State the blood parasite species.
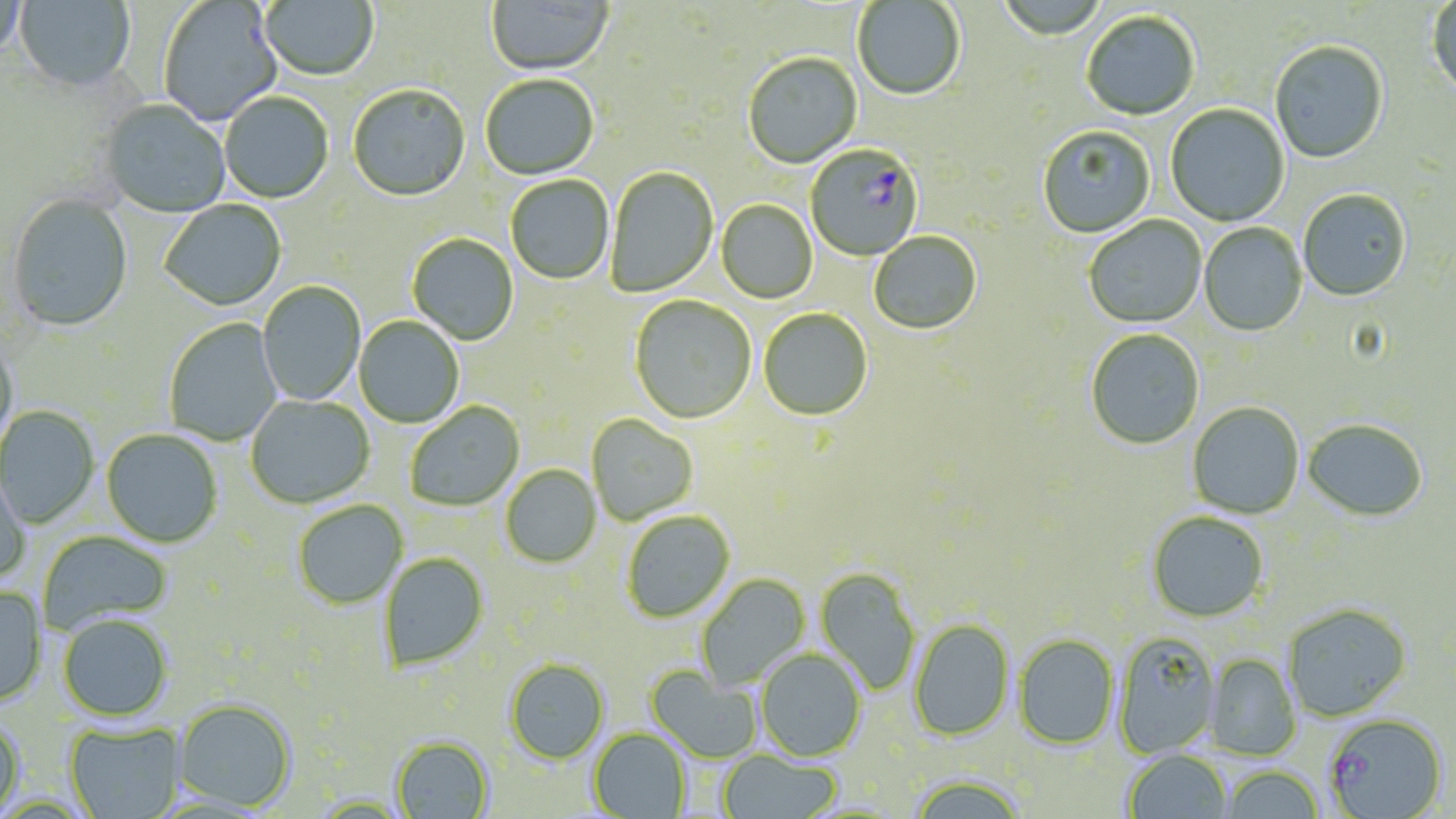
Plasmodium falciparum.

Approximate bounding boxes as [x1, y1, x2, y2] in pixels. Uninfected red blood cell locations: [15, 0, 136, 94], [260, 0, 378, 83], [995, 0, 1109, 43], [1426, 0, 1456, 99], [0, 1, 28, 63], [159, 1, 283, 127], [487, 1, 614, 78], [853, 1, 966, 103], [1081, 12, 1200, 122], [1270, 43, 1388, 165], [743, 54, 862, 169], [481, 76, 599, 181], [348, 86, 470, 203], [220, 93, 334, 204], [99, 100, 231, 219], [1165, 105, 1290, 227], [1037, 127, 1156, 239], [606, 167, 718, 298], [506, 176, 614, 286], [1298, 190, 1411, 302], [6, 194, 133, 334], [160, 200, 287, 312], [716, 200, 818, 305], [1083, 216, 1207, 329], [1198, 223, 1307, 337], [869, 232, 982, 336], [407, 234, 518, 346], [257, 281, 366, 406], [629, 296, 757, 425], [758, 309, 872, 421], [354, 316, 464, 429], [163, 319, 282, 446], [1086, 330, 1204, 450], [0, 336, 19, 454], [245, 395, 375, 510], [406, 402, 525, 512], [1187, 403, 1304, 519], [0, 406, 99, 530], [586, 414, 699, 526], [1302, 419, 1428, 523], [101, 429, 223, 548], [501, 465, 601, 569], [0, 467, 30, 587], [293, 501, 408, 610], [622, 511, 735, 624], [1147, 512, 1268, 623], [37, 531, 172, 634], [379, 553, 490, 672], [815, 567, 921, 694], [696, 573, 811, 692], [0, 585, 47, 708], [1282, 603, 1412, 722], [57, 614, 173, 722], [908, 619, 1014, 741], [1113, 632, 1221, 758], [1013, 635, 1119, 749], [755, 649, 867, 762], [1205, 654, 1301, 760], [504, 659, 609, 764], [646, 665, 764, 763], [173, 699, 297, 812], [0, 715, 25, 818], [65, 721, 185, 819], [588, 728, 692, 818], [391, 736, 493, 819], [1124, 749, 1232, 818], [717, 751, 843, 818], [1220, 765, 1324, 819], [907, 775, 1028, 819]. Plasmodium falciparum-infected red blood cell locations: [806, 145, 924, 261], [1323, 713, 1448, 818]. May-Grünwald-Giemsa-stained preparation. Thin blood smear. Image is 1456×819 pixels. 1000x magnification. Light microscopy. Single field of view.